Report the malaria status of this cell.
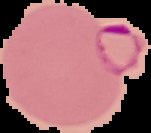

It is parasitized.

From a thin blood film. Image is 151×133 pixels. The area outside the segmented cell region is set to black.